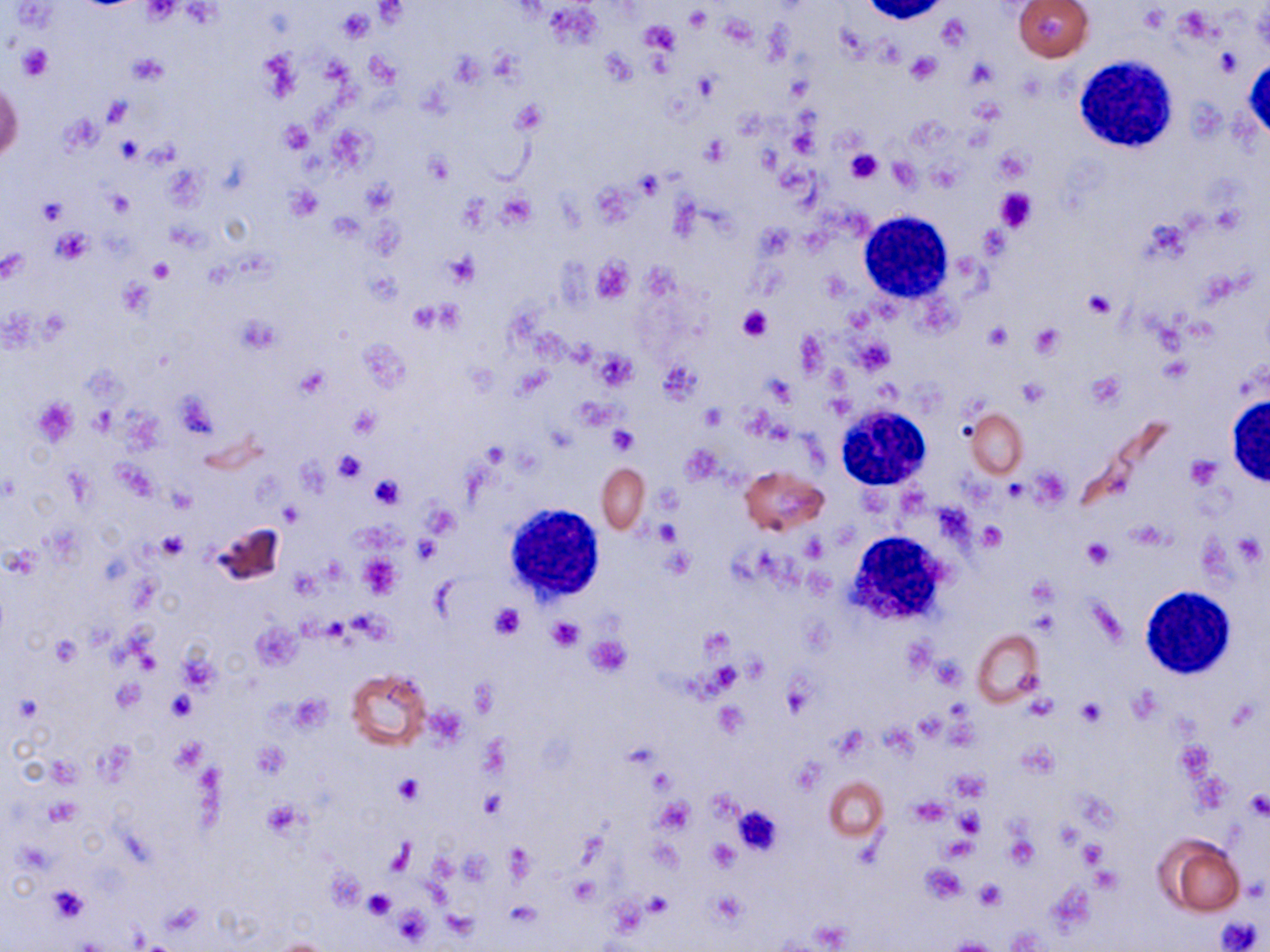

Approximate bounding boxes as (x1,y1)-(x2,y2) corner pairs in pixels. Platelet locations: (142,1)-(184,25), (375,1)-(408,26), (682,6)-(712,33), (338,9)-(374,42), (641,20)-(680,54), (18,44)-(52,81), (1214,48)-(1240,77), (258,50)-(302,99), (906,52)-(942,82), (127,53)-(169,85), (964,61)-(997,88), (101,99)-(131,128), (513,99)-(545,134), (279,121)-(312,153), (117,135)-(142,161), (700,135)-(730,165), (845,149)-(882,185), (994,149)-(1030,181), (426,153)-(453,185), (286,184)-(322,220), (994,187)-(1037,231), (107,188)-(133,216), (497,194)-(534,228), (39,198)-(66,224), (979,225)-(1010,259), (53,229)-(92,263), (445,252)-(480,288), (591,256)-(634,303), (150,259)-(173,284), (1083,289)-(1116,319), (737,304)-(773,342), (984,321)-(1012,350), (1030,325)-(1063,356), (852,337)-(894,375), (594,349)-(636,386), (1162,357)-(1192,382), (294,368)-(329,401), (764,374)-(796,403), (1015,380)-(1050,409), (33,398)-(79,446), (698,404)-(725,428), (347,407)-(379,438), (608,426)-(636,454), (333,451)-(367,481), (1187,456)-(1219,486), (1027,468)-(1069,506), (370,475)-(402,509), (1002,480)-(1030,502), (656,521)-(682,545), (980,521)-(1008,550), (157,531)-(189,557), (802,532)-(827,558), (412,538)-(440,563), (1082,538)-(1114,570), (663,547)-(694,578), (359,557)-(400,597), (490,604)-(526,638), (548,617)-(584,650), (52,636)-(80,667), (586,637)-(630,676), (166,693)-(196,721), (14,696)-(40,723), (1077,699)-(1106,726), (714,702)-(750,737), (172,738)-(207,771), (1177,743)-(1212,778), (394,774)-(423,804), (1244,791)-(1268,820), (479,792)-(505,818), (45,797)-(79,825), (908,799)-(951,827), (261,800)-(301,837), (733,806)-(782,853), (957,810)-(981,835), (707,838)-(740,871), (1079,840)-(1104,868), (922,866)-(966,902), (973,878)-(1006,910), (48,885)-(87,922), (363,889)-(394,919), (643,892)-(672,917), (392,908)-(431,945), (1214,916)-(1264,952), (811,923)-(849,950). Uninfected red blood cell locations: (1012,0)-(1094,62), (0,81)-(24,165), (851,336)-(895,375), (966,409)-(1028,480), (597,463)-(650,534), (739,465)-(830,535), (215,522)-(286,584), (972,630)-(1045,707), (346,668)-(432,749), (823,776)-(889,842), (1155,835)-(1247,917), (267,938)-(337,951). White blood cell locations: (1075,55)-(1178,154), (855,210)-(952,304), (1227,393)-(1270,486), (836,406)-(931,490), (506,503)-(605,601), (845,530)-(952,625), (1141,586)-(1235,678). Slide-level diagnosis: negative for blood parasites. Thin blood film. Image is 1270×952 pixels. May-Grünwald-Giemsa-stained preparation. Single field of view. Captured at 1000x magnification. Optical microscopy.